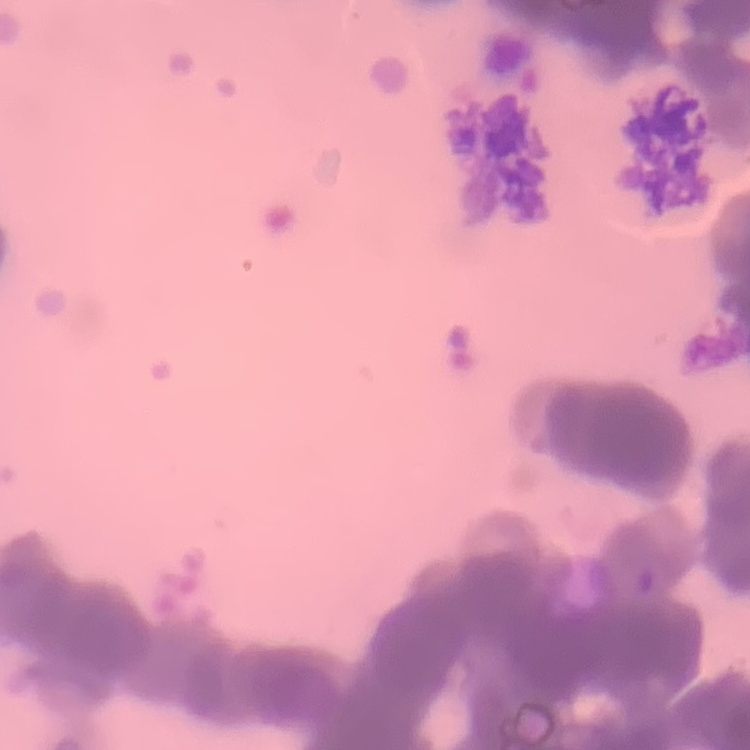

Summary:
  - Red blood cell morphology: rouleaux formation
  - Preparation: thin peripheral smear
  - Stain: Field's or Giemsa
  - Image type: one tile cut from a larger photomicrograph